Locate every leukocyte (white blood cell).
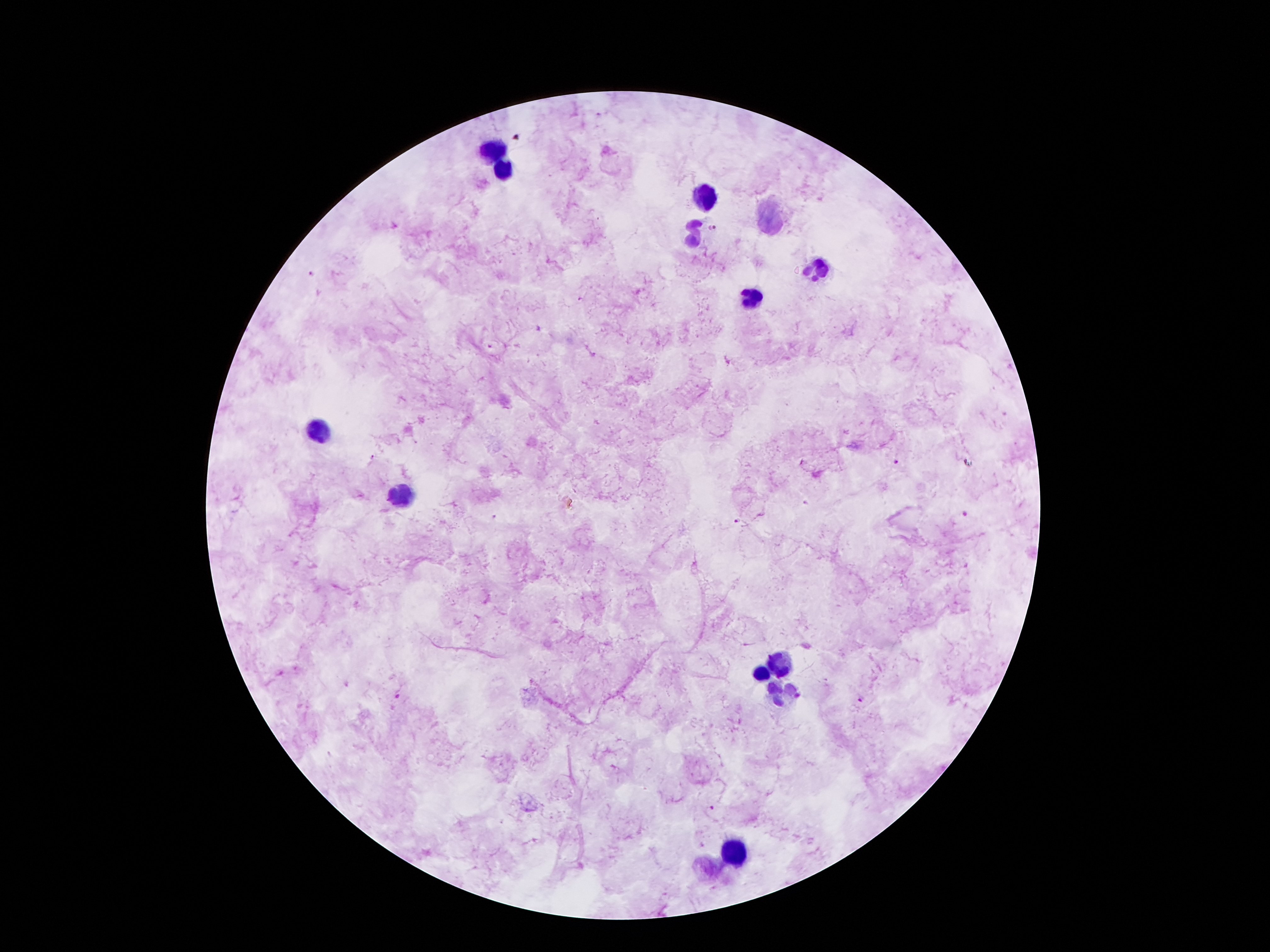
Approximate centers as (x, y) in pixels.
Leukocytes: (492, 149), (502, 169), (704, 195), (770, 214), (695, 231), (819, 268), (751, 296), (320, 427), (404, 494), (781, 665), (760, 676), (786, 699), (735, 853).

Summary:
  - Malaria parasite locations: (711, 228), (311, 273), (490, 348), (372, 457), (894, 462), (806, 503), (965, 513), (493, 516), (736, 521), (397, 696), (860, 700), (711, 809)
  - Magnification: 100x
  - Image size: 1270×952 pixels
  - Stain: Giemsa
  - Field of view: single
  - Preparation: thick peripheral-blood smear
  - Patient malaria status: positive for Plasmodium falciparum
  - Capture: smartphone camera through the microscope eyepiece